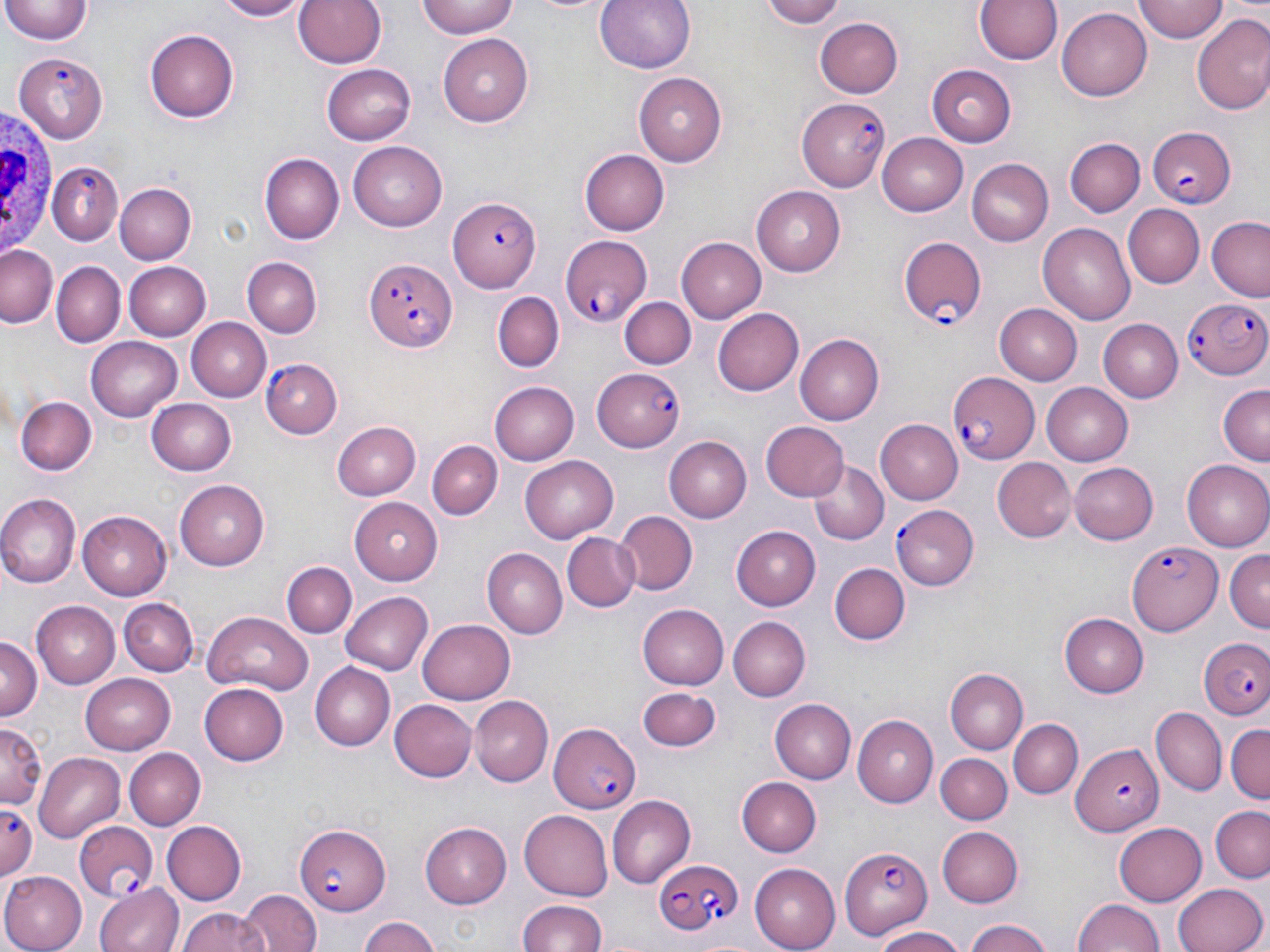

slide-level diagnosis = Plasmodium falciparum
stain = May-Grünwald-Giemsa
magnification = 1000x
modality = optical microscopy
Plasmodium falciparum-infected red blood cell locations = approximate bounding boxes as (x1, y1, x2, y2) in pixels: (14, 50, 109, 140), (799, 97, 892, 191), (1149, 126, 1235, 207), (49, 162, 123, 242), (450, 198, 540, 292), (559, 232, 655, 326), (898, 237, 986, 328), (365, 255, 459, 350), (1182, 297, 1270, 380), (263, 360, 341, 439), (592, 365, 687, 451), (947, 372, 1038, 464), (891, 505, 977, 588), (1128, 541, 1224, 636), (1200, 636, 1270, 719), (549, 726, 641, 815), (1070, 745, 1163, 835), (0, 801, 39, 881), (74, 821, 160, 899), (294, 822, 390, 914), (838, 841, 933, 939), (652, 858, 741, 934)
white blood cell locations = approximate bounding boxes as (x1, y1, x2, y2) in pixels: (0, 106, 57, 260)
image size = 1270×952 pixels
preparation = thin blood film
field of view = single
uninfected red blood cell locations = approximate bounding boxes as (x1, y1, x2, y2) in pixels: (211, 0, 313, 21), (293, 0, 386, 70), (417, 0, 519, 39), (516, 0, 618, 15), (594, 0, 694, 76), (758, 0, 849, 27), (972, 0, 1064, 67), (1135, 0, 1228, 42), (3, 1, 92, 45), (1057, 8, 1153, 100), (1192, 14, 1270, 114), (816, 18, 906, 97), (145, 28, 240, 121), (438, 32, 534, 123), (323, 64, 416, 144), (928, 66, 1016, 147), (635, 72, 726, 166), (877, 131, 969, 218), (1064, 138, 1144, 217), (349, 140, 451, 231), (580, 150, 670, 234), (262, 152, 345, 243), (965, 159, 1053, 247), (114, 184, 194, 265), (752, 187, 846, 276), (1124, 205, 1204, 288), (1206, 218, 1270, 300), (1037, 222, 1136, 323), (676, 236, 766, 323), (2, 244, 60, 327), (243, 257, 322, 337), (124, 261, 209, 339), (51, 262, 125, 346), (492, 290, 565, 371), (621, 295, 695, 368), (994, 303, 1082, 385), (713, 308, 804, 397), (185, 316, 271, 401), (1097, 320, 1183, 402), (796, 335, 885, 424), (86, 336, 182, 420), (488, 381, 579, 466), (1041, 382, 1133, 465), (1218, 385, 1270, 464), (16, 394, 96, 476), (148, 397, 240, 474), (876, 419, 962, 504), (759, 421, 847, 502), (330, 422, 420, 500), (664, 437, 750, 523), (428, 441, 501, 520), (520, 454, 620, 543), (995, 457, 1075, 543), (807, 459, 888, 547), (1183, 460, 1270, 551), (1069, 461, 1158, 544), (174, 480, 270, 571), (0, 494, 81, 585), (347, 498, 444, 585), (78, 511, 171, 600), (615, 512, 697, 596), (731, 526, 820, 610), (561, 531, 638, 612), (485, 548, 567, 638), (1225, 550, 1269, 631), (283, 559, 355, 639), (830, 562, 909, 645), (341, 590, 432, 675), (120, 598, 197, 677), (30, 600, 119, 688), (640, 604, 729, 689), (201, 611, 312, 694), (1060, 613, 1149, 695), (727, 616, 810, 701), (418, 618, 516, 703), (0, 635, 40, 723), (312, 661, 397, 750), (946, 667, 1026, 752), (81, 673, 176, 753), (199, 683, 289, 766), (640, 688, 722, 753), (472, 696, 552, 785), (391, 699, 477, 782), (772, 699, 856, 783), (1152, 707, 1225, 796), (852, 715, 938, 807), (1010, 718, 1083, 799), (1, 719, 46, 807), (1226, 722, 1269, 804), (123, 748, 206, 829), (35, 752, 123, 840), (936, 753, 1011, 824), (738, 777, 820, 856), (606, 796, 695, 886), (1209, 807, 1270, 883), (518, 808, 612, 897), (161, 820, 244, 906), (1116, 821, 1209, 906), (422, 823, 510, 907), (936, 825, 1024, 906), (749, 864, 840, 951), (0, 871, 87, 952), (96, 881, 183, 952), (1172, 881, 1267, 952), (238, 890, 319, 952), (1073, 897, 1166, 951), (516, 899, 606, 952), (177, 906, 269, 952), (357, 915, 440, 952), (962, 919, 1057, 952), (870, 925, 967, 952)